Name the parasite shown.
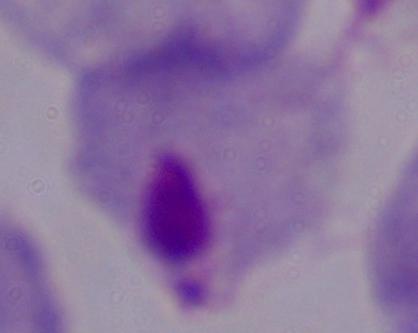
This is a trichomonad.

modality = photomicrograph
magnification = 1000x